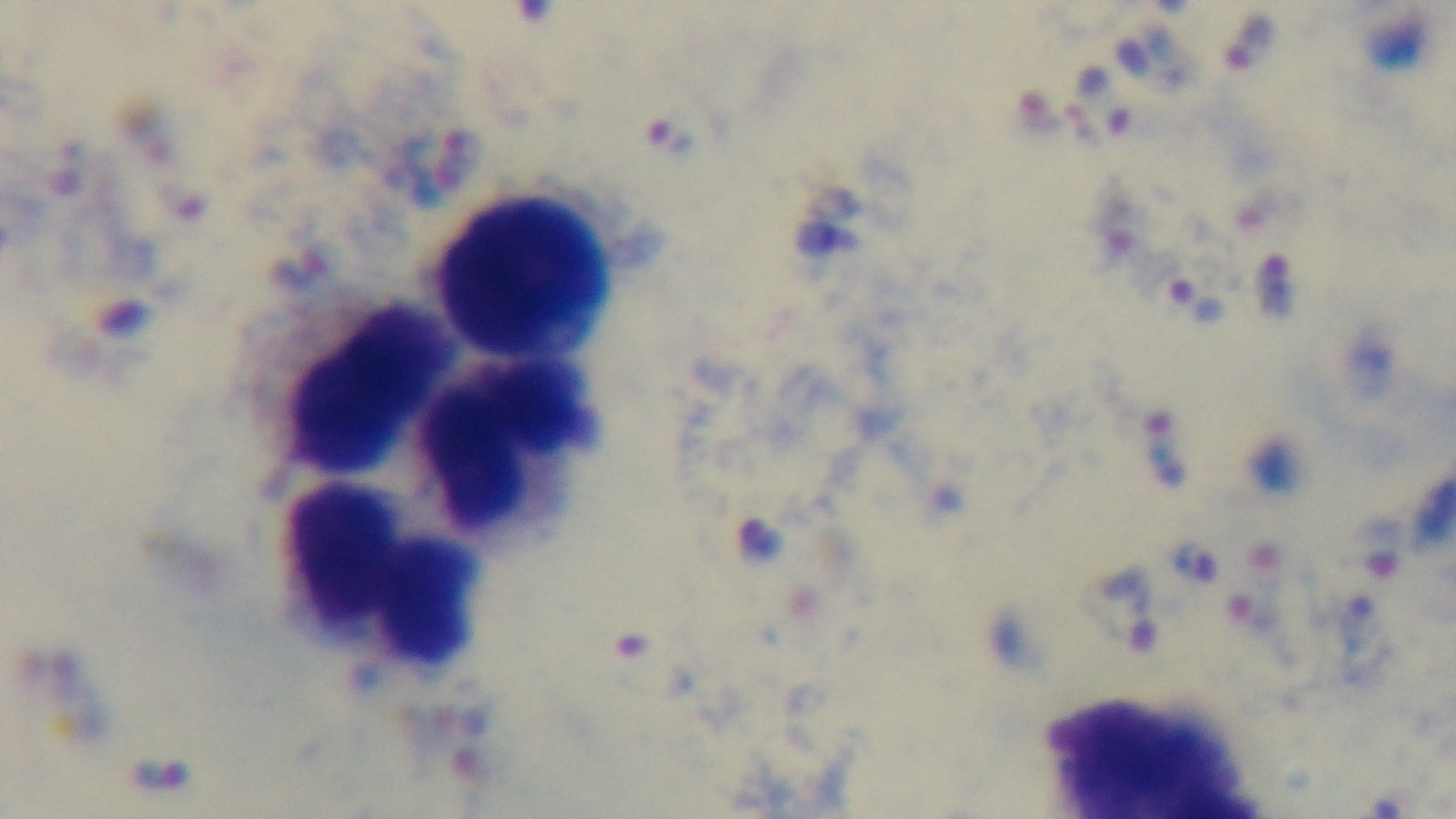 Single field of view. Mounted 4K digital camera. Giemsa-stained. Preparation: thick smear. Photomicrograph. 100x oil-immersion objective. Malaria status: infected.